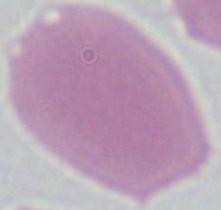

An erythrocyte is shown. Micrograph. Captured at 1000x magnification.